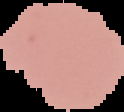
From a thin blood smear. The area outside the segmented cell region is set to black. Image is 124×112 pixels. Result: negative for Plasmodium parasites.